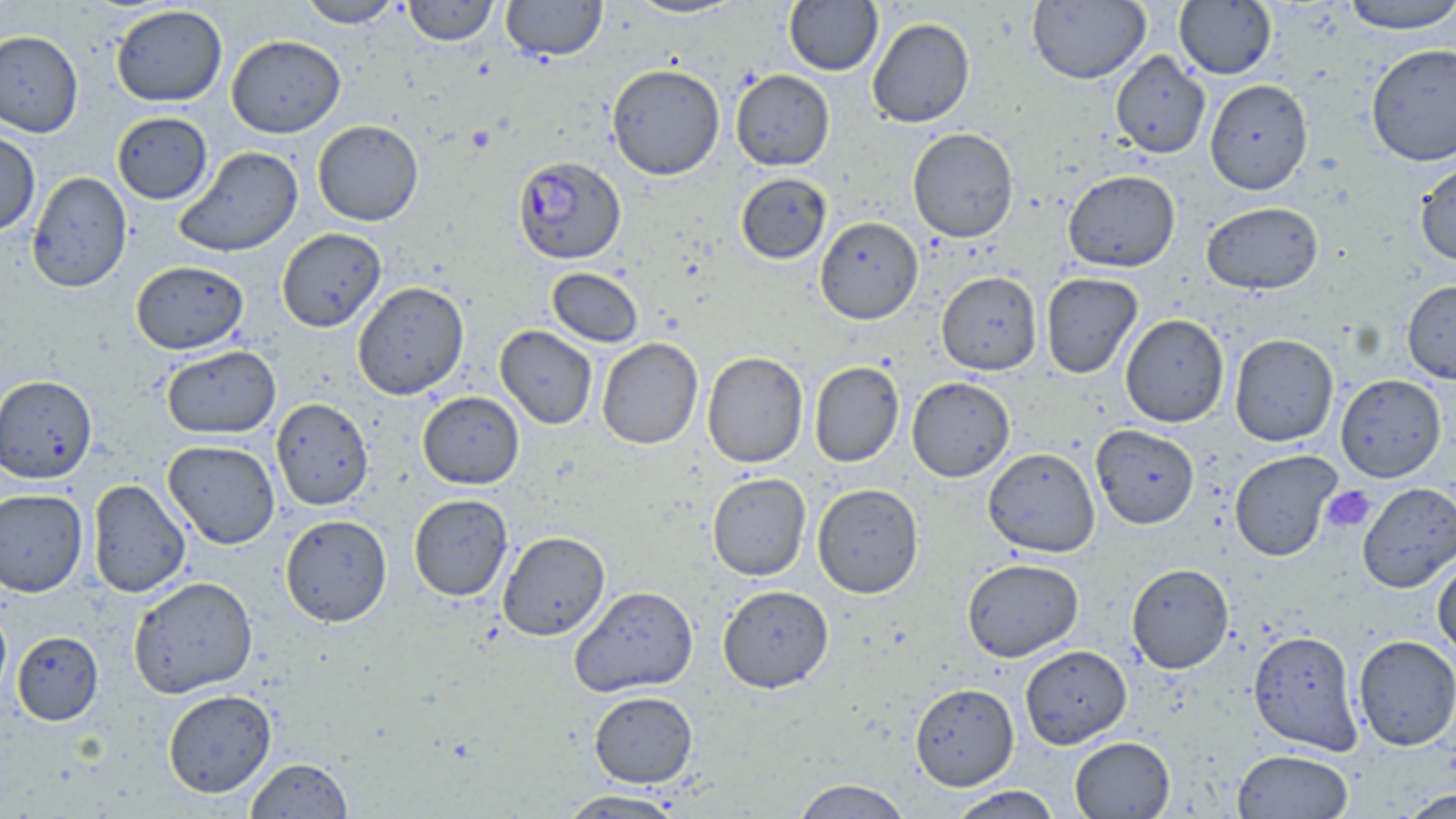

Summary:
  - Coordinate format: approximate bounding boxes as [x1, y1, x2, y2] in pixels
  - Uninfected red blood cell locations: [297, 0, 404, 28], [402, 0, 499, 46], [500, 0, 608, 62], [625, 0, 746, 19], [1027, 0, 1151, 85], [784, 1, 883, 75], [1174, 1, 1277, 79], [1341, 1, 1455, 34], [110, 4, 228, 107], [867, 17, 975, 128], [0, 30, 83, 137], [226, 34, 346, 138], [1366, 43, 1456, 166], [1110, 51, 1211, 159], [606, 63, 725, 180], [730, 69, 835, 171], [1205, 79, 1314, 195], [112, 112, 213, 204], [312, 119, 424, 226], [907, 127, 1019, 243], [0, 130, 41, 237], [175, 146, 303, 257], [1414, 159, 1456, 267], [1063, 170, 1180, 272], [26, 171, 132, 293], [735, 172, 832, 264], [1201, 201, 1323, 294], [815, 216, 923, 325], [277, 228, 387, 332], [131, 260, 249, 354], [547, 268, 644, 347], [936, 271, 1042, 375], [1040, 272, 1143, 378], [1402, 279, 1456, 384], [352, 282, 469, 400], [1120, 314, 1229, 427], [495, 325, 598, 430], [1229, 333, 1339, 447], [596, 337, 703, 450], [161, 345, 281, 439], [701, 351, 809, 468], [809, 361, 904, 467], [0, 374, 97, 484], [1336, 374, 1446, 482], [907, 377, 1015, 482], [417, 391, 524, 489], [270, 397, 374, 511], [1090, 424, 1200, 529], [163, 440, 280, 549], [983, 448, 1100, 557], [1229, 450, 1341, 561], [707, 472, 811, 581], [87, 479, 191, 597], [1357, 482, 1456, 593], [812, 483, 924, 598], [0, 488, 88, 596], [408, 494, 513, 601], [280, 514, 392, 627], [497, 530, 610, 641], [1432, 556, 1456, 661], [963, 559, 1084, 662], [1126, 562, 1234, 673], [128, 576, 259, 699], [718, 584, 834, 692], [570, 585, 698, 697], [0, 603, 12, 707], [1248, 630, 1363, 756], [12, 631, 103, 725], [1353, 635, 1456, 751], [1020, 645, 1132, 749], [910, 683, 1019, 790], [163, 689, 277, 798], [588, 690, 698, 787], [1069, 736, 1176, 818], [1232, 749, 1354, 819], [245, 757, 354, 818], [791, 779, 913, 819], [947, 785, 1062, 819], [1397, 789, 1455, 818], [556, 790, 688, 818]
  - Plasmodium falciparum-infected red blood cell locations: [513, 156, 627, 265]
  - Platelet locations: [466, 127, 494, 152], [1321, 485, 1376, 533]
  - Slide-level diagnosis: Plasmodium falciparum
  - Modality: light microscopy
  - Preparation: thin blood smear
  - Field of view: one of a larger specimen
  - Magnification: 1000x
  - Image size: 1456×819 pixels
  - Stain: May-Grünwald-Giemsa